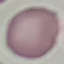

malaria status = uninfected
stain = Giemsa
capture = smartphone through the microscope eyepiece
image type = cell patch, automatically extracted from a larger field of view and resized to 64 × 64 pixels
preparation = thin blood smear